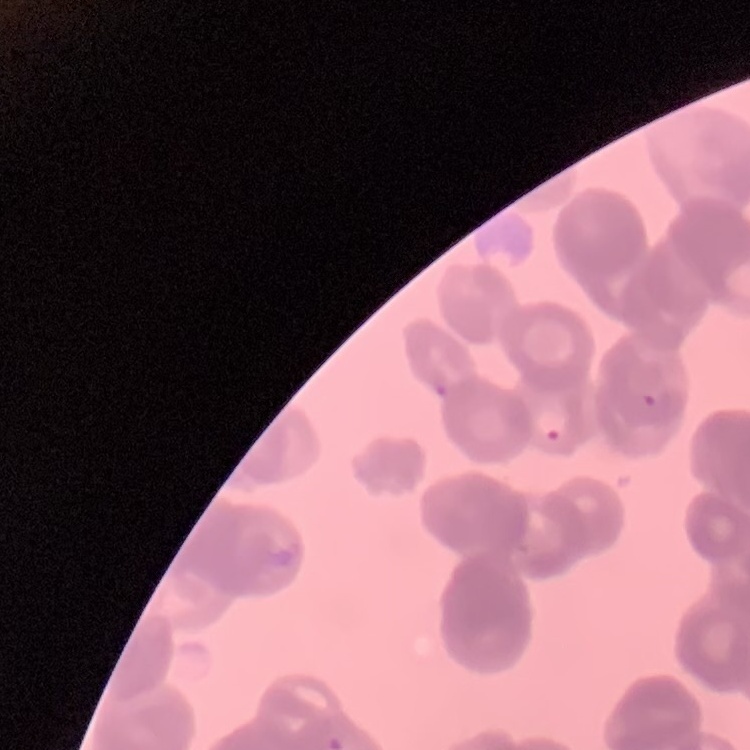

Summary:
  - Erythrocyte morphology: rouleaux formation
  - Stain: Field's or Giemsa
  - Preparation: thin peripheral smear
  - Image type: square crop of a larger photomicrograph